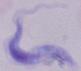

Summary:
  - Magnification: 1000x
  - Modality: micrograph
  - Identification: trypanosome